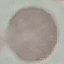
result = negative for malaria parasites
capture = smartphone through the microscope eyepiece
stain = Giemsa
image type = cell patch, automatically extracted from a larger field of view and resized to 64 × 64 pixels
preparation = thin blood smear